Point out each leukocyte.
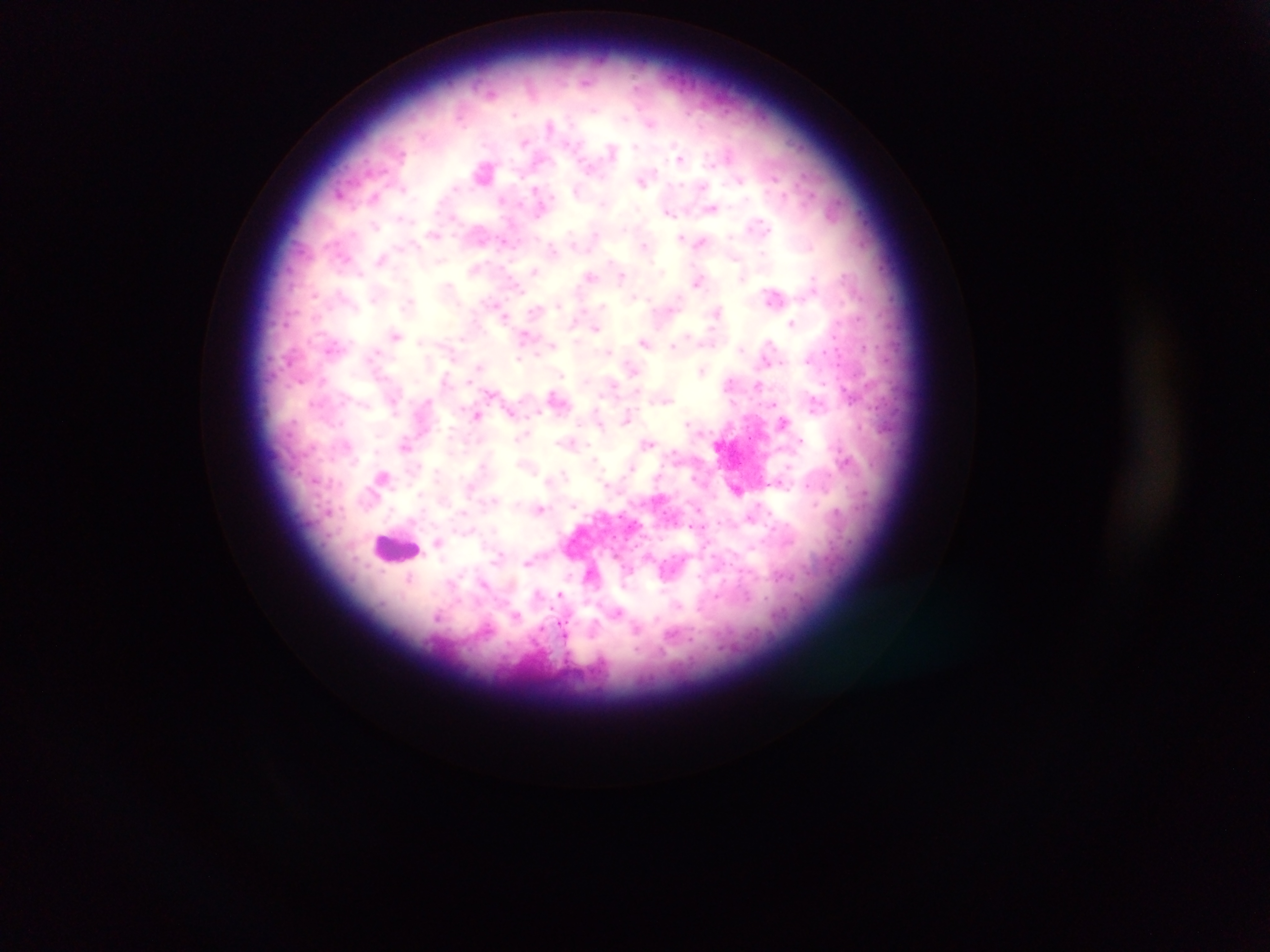
Approximate centers as (x, y) in pixels.
Leukocytes: (396, 547).

Malaria parasite locations: (587, 82), (490, 92), (514, 115), (650, 124), (549, 125), (524, 143), (635, 146), (612, 150), (680, 158), (483, 172), (739, 180), (642, 181), (457, 187), (537, 189), (404, 190), (374, 197), (501, 199), (603, 204), (712, 208), (668, 212), (401, 217), (453, 218), (758, 224), (376, 226), (595, 233), (434, 234), (732, 236), (681, 237), (700, 242), (645, 245), (415, 247), (553, 249), (762, 252), (345, 257), (737, 258), (381, 259), (441, 260), (611, 261), (535, 270), (360, 274), (590, 276), (622, 277), (813, 278), (698, 282), (448, 286), (518, 289), (340, 293), (314, 295), (773, 296), (634, 297), (373, 300), (408, 302), (558, 305), (603, 306), (716, 311), (505, 316), (792, 323), (596, 329), (396, 335), (524, 335), (463, 338), (769, 341), (420, 342), (644, 342), (552, 345), (674, 346), (864, 346), (332, 347), (740, 347), (609, 350), (376, 352), (823, 352), (519, 358), (806, 360), (782, 361), (478, 367), (632, 369), (702, 371), (560, 374), (299, 381), (323, 381), (469, 381), (729, 382), (823, 384), (757, 385), (613, 386), (489, 393), (427, 400), (666, 401), (313, 404), (774, 404), (538, 411), (596, 411), (394, 412), (512, 414), (477, 415), (627, 417), (340, 422), (687, 422), (784, 422), (861, 426), (378, 434), (523, 434), (518, 438), (801, 441), (570, 442), (648, 442), (467, 443), (405, 446), (377, 449), (673, 452), (594, 460), (355, 461), (483, 465), (418, 466), (789, 466), (631, 467), (564, 473), (437, 474), (315, 480), (547, 480), (777, 482), (606, 485), (806, 486), (419, 494), (494, 499), (816, 504), (573, 505), (540, 508), (462, 512), (770, 513), (750, 518), (718, 521), (692, 526), (437, 542), (500, 554), (526, 563), (410, 578), (484, 584), (538, 592), (560, 594), (678, 605), (618, 612), (516, 615), (438, 617), (657, 618), (562, 626). Photographed through a microscope with a mobile-phone camera. Thick blood film. One field of view. Image is 1270×952 pixels. Sample from Ghana.